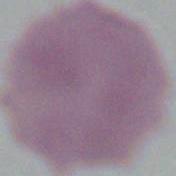

1000x magnification. Photomicrograph. An erythrocyte is shown.